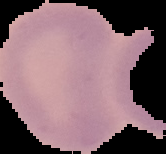
Summary:
  - Preparation: thin blood smear
  - Image size: 166×154 pixels
  - Result: no Plasmodium parasites seen
  - Image type: segmented cell region on a black background